Comment on the morphology of the red blood cells.
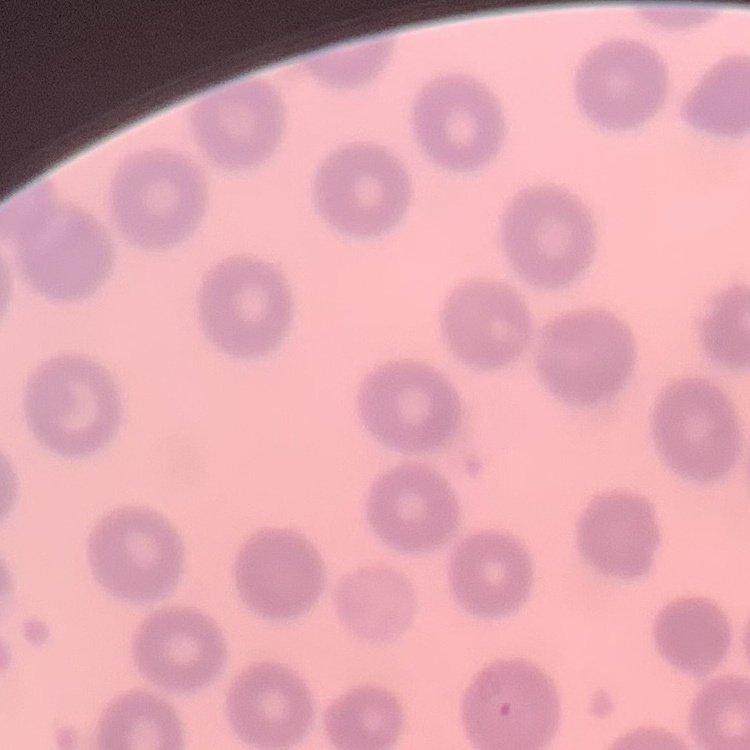

They show no rouleaux formation.

One tile cut from a larger photomicrograph. Field's or Giemsa stain. Thin blood smear.